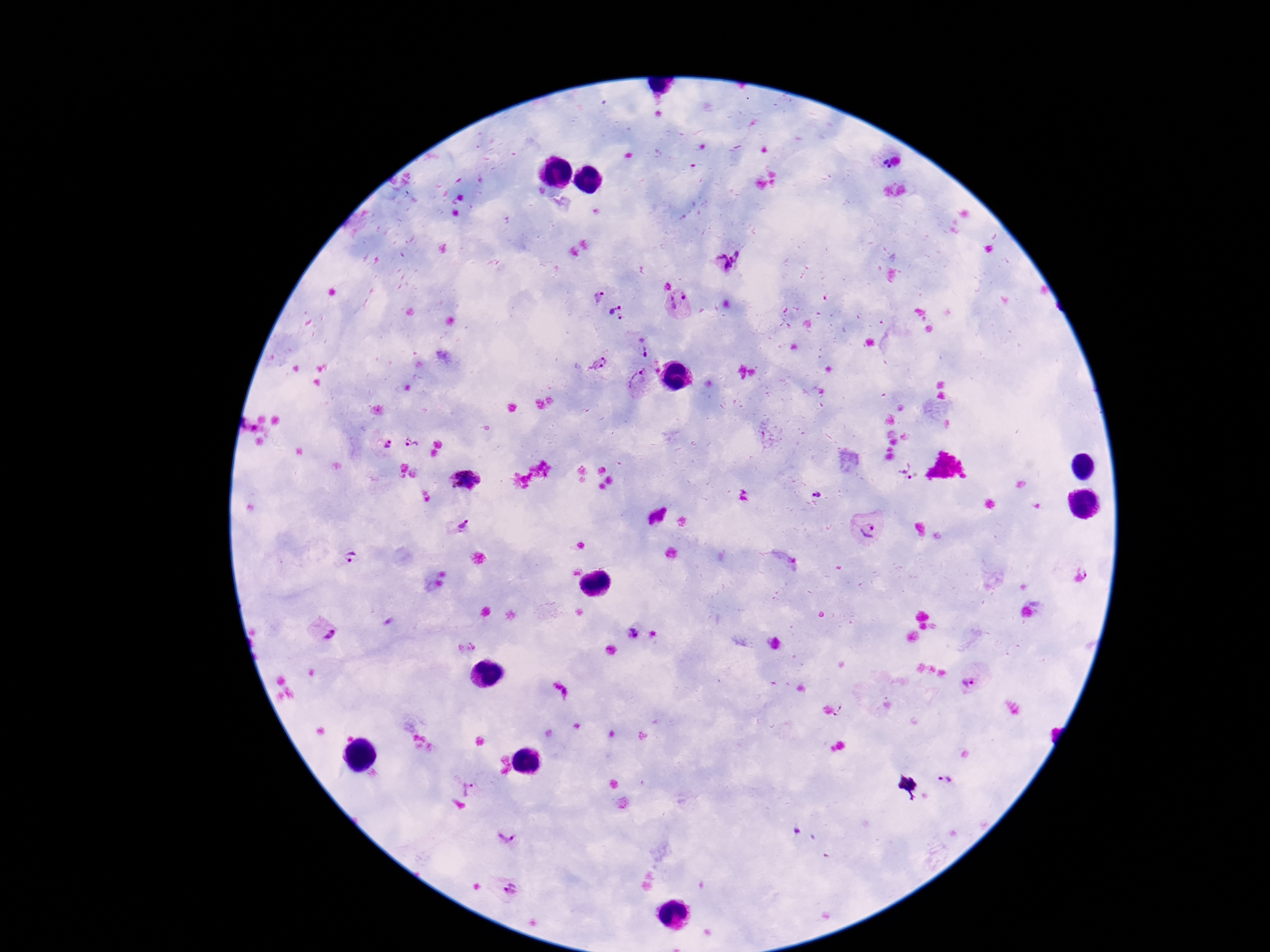
Approximate centers as [x, y] in pixels.
Summary:
  - Plasmodium parasite locations: [728, 258], [599, 295], [683, 305], [617, 313], [644, 345], [600, 362], [640, 380], [415, 441], [387, 444], [909, 472], [464, 477], [816, 495], [461, 526], [867, 529], [351, 555], [325, 631], [633, 632], [976, 679], [943, 779], [466, 787], [509, 832], [507, 887]
  - Stain: Giemsa
  - Preparation: thick blood film
  - Field of view: single
  - Magnification: 100x
  - Capture: smartphone camera through the microscope eyepiece
  - Patient malaria status: positive
  - Image size: 1270×952 pixels